Report the malaria status of this cell.
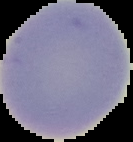
Uninfected.

image type = cell region segmented out of the field of view; surrounding area masked to black
preparation = thin blood smear
image size = 133×142 pixels